Assess this cell for malaria.
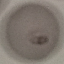
Uninfected.

capture = smartphone camera at the microscope eyepiece
stain = Giemsa
image type = automatically extracted cell patch, resized to 64 × 64 pixels
preparation = thin blood smear